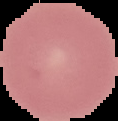

Summary:
  - Image type: segmented cell region on a black background
  - Result: no malaria parasites detected
  - Image size: 118×121 pixels
  - Preparation: thin blood smear